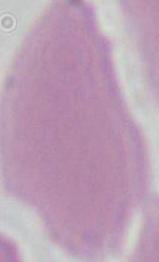
modality: micrograph
magnification: 1000x
identification: red blood cell